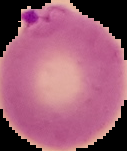

malaria status = parasitized
preparation = thin blood smear
image size = 127×151 pixels
image type = segmented cell region on a black background